Locate every Plasmodium parasite.
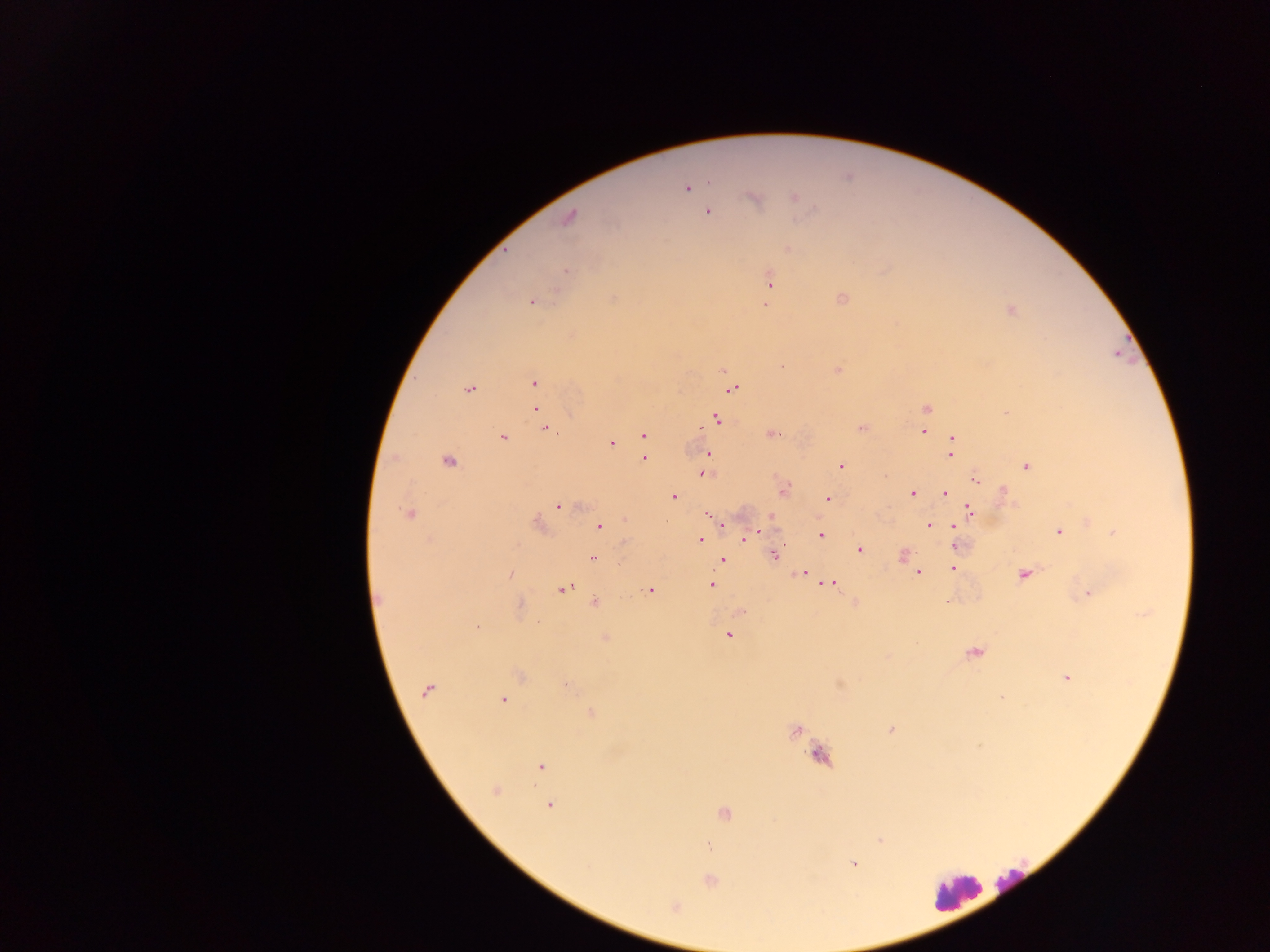
Approximate centers as x y in pixels.
Plasmodium parasites: 686 188; 754 197; 794 197; 708 212; 568 217; 788 248; 567 271; 770 282; 841 297; 531 302; 766 304; 1010 310; 837 369; 723 370; 534 382; 470 388; 730 388; 535 408; 926 408; 1006 413; 716 419; 926 420; 545 428; 861 428; 923 431; 772 433; 644 434; 502 438; 952 440; 610 443; 950 452; 708 454; 643 457; 448 461; 705 465; 840 465; 1026 465; 703 472; 884 474; 975 479; 783 488; 912 493; 944 493; 1004 493; 672 496; 828 498; 560 505; 968 510; 409 513; 709 515; 770 516; 1087 520; 537 523; 721 524; 929 525; 598 526; 1058 531; 759 532; 1114 533; 954 534; 820 535; 742 539; 700 540; 955 545; 859 549; 773 554; 901 554; 593 558; 722 559; 954 568; 916 569; 803 572; 918 572; 1024 573; 510 575; 830 583; 710 584; 563 587; 649 590; 1087 592; 594 602; 946 602; 855 603; 519 606; 739 611; 478 627; 728 635; 605 638; 974 652; 519 675; 1066 677; 567 685; 427 690; 1002 696; 503 700; 591 713; 795 729; 891 729; 541 766; 495 790; 549 805; 724 813; 879 839; 709 845; 853 863; 710 880; 674 906.

Summary:
  - Leukocyte locations: 820 756; 1013 877; 956 891
  - Capture: mobile-phone photograph through a microscope
  - Preparation: thick blood film
  - Image size: 1270×952 pixels
  - Country: Ghana
  - Field of view: single